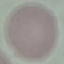
Summary:
  - Malaria status: uninfected
  - Preparation: thin blood film
  - Stain: Giemsa
  - Image type: cell patch, automatically extracted from a larger field of view and resized to 64 × 64 pixels
  - Capture: smartphone through the microscope eyepiece